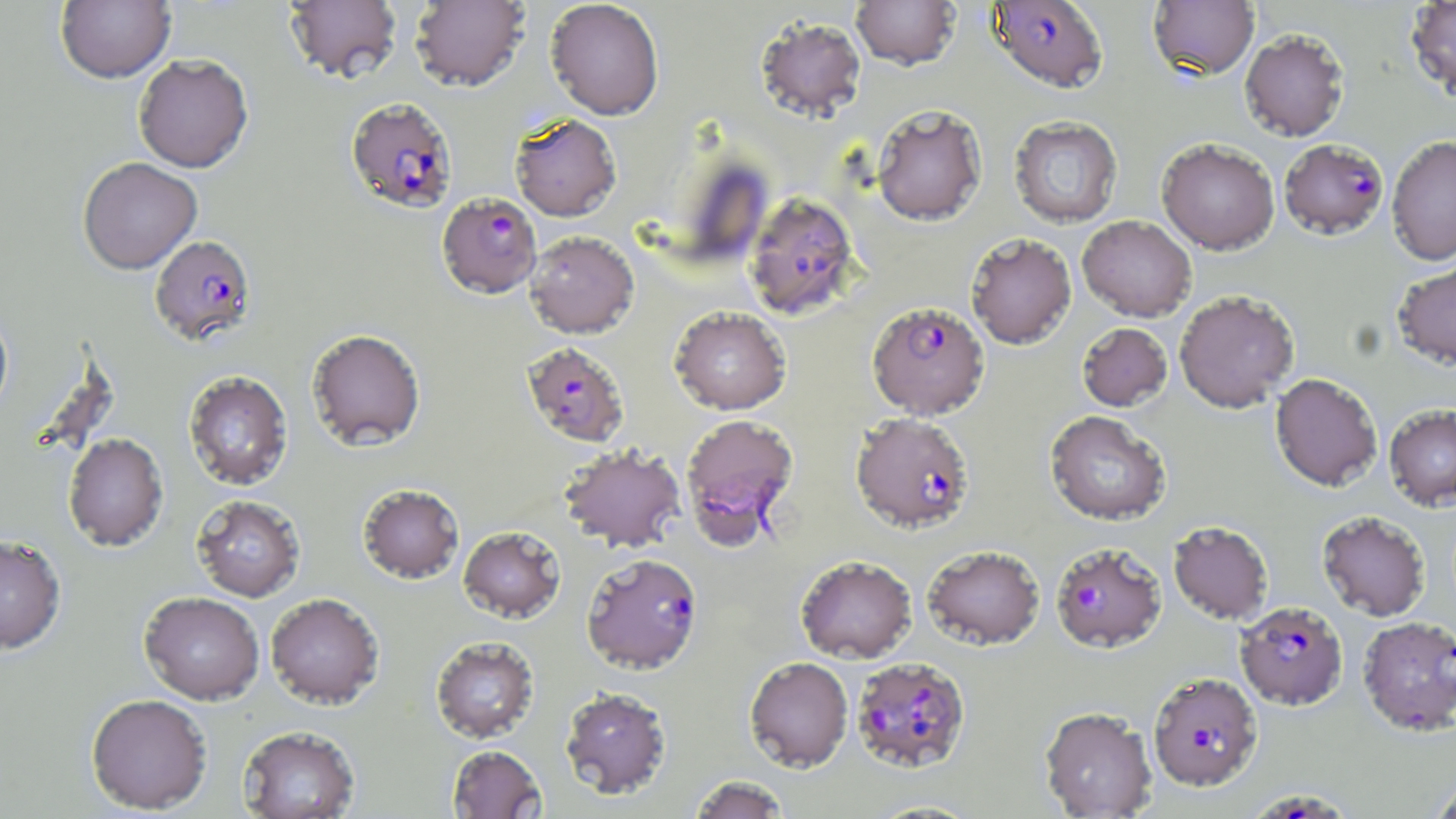
Approximate bounding boxes as [x1, y1, x2, y2] in pixels. Uninfected red blood cell locations: [56, 0, 176, 83], [284, 0, 402, 85], [545, 0, 665, 120], [851, 0, 961, 70], [1405, 0, 1456, 101], [409, 1, 530, 92], [1148, 1, 1259, 80], [755, 16, 866, 122], [1240, 28, 1350, 142], [133, 53, 253, 173], [872, 105, 987, 227], [509, 114, 621, 221], [1009, 116, 1123, 228], [1386, 135, 1456, 266], [1156, 138, 1280, 255], [77, 157, 202, 274], [1077, 215, 1196, 322], [525, 231, 639, 339], [966, 233, 1077, 348], [1392, 258, 1456, 372], [1174, 290, 1300, 413], [669, 306, 791, 414], [0, 307, 13, 421], [1077, 323, 1172, 411], [307, 328, 426, 451], [183, 370, 294, 490], [1270, 373, 1383, 493], [1384, 404, 1456, 511], [1044, 411, 1171, 526], [63, 432, 169, 550], [559, 445, 685, 553], [357, 483, 464, 584], [191, 494, 306, 602], [1317, 511, 1431, 622], [1168, 521, 1274, 625], [458, 525, 566, 623], [0, 534, 66, 654], [922, 546, 1045, 651], [795, 555, 917, 663], [139, 592, 264, 705], [265, 593, 385, 710], [430, 636, 540, 744], [744, 656, 853, 772], [559, 687, 672, 800], [86, 693, 213, 814], [1039, 706, 1157, 818], [237, 725, 360, 819], [447, 745, 547, 818], [688, 775, 791, 819], [1427, 775, 1456, 819], [864, 799, 985, 818]. Plasmodium falciparum-infected red blood cell locations: [987, 0, 1109, 92], [345, 96, 458, 213], [1279, 138, 1389, 239], [437, 192, 542, 299], [744, 192, 861, 321], [149, 235, 257, 346], [867, 301, 989, 419], [521, 342, 630, 447], [850, 413, 975, 535], [680, 414, 800, 548], [1050, 542, 1167, 653], [582, 553, 703, 674], [1235, 602, 1348, 711], [1357, 616, 1456, 738], [851, 657, 972, 774], [1148, 673, 1262, 792], [1253, 793, 1349, 819]. Slide-level diagnosis: Plasmodium falciparum. May-Grünwald-Giemsa-stained preparation. Light microscopy. Single field of view. Image is 1456×819 pixels. Captured at 1000x magnification. Thin blood smear.